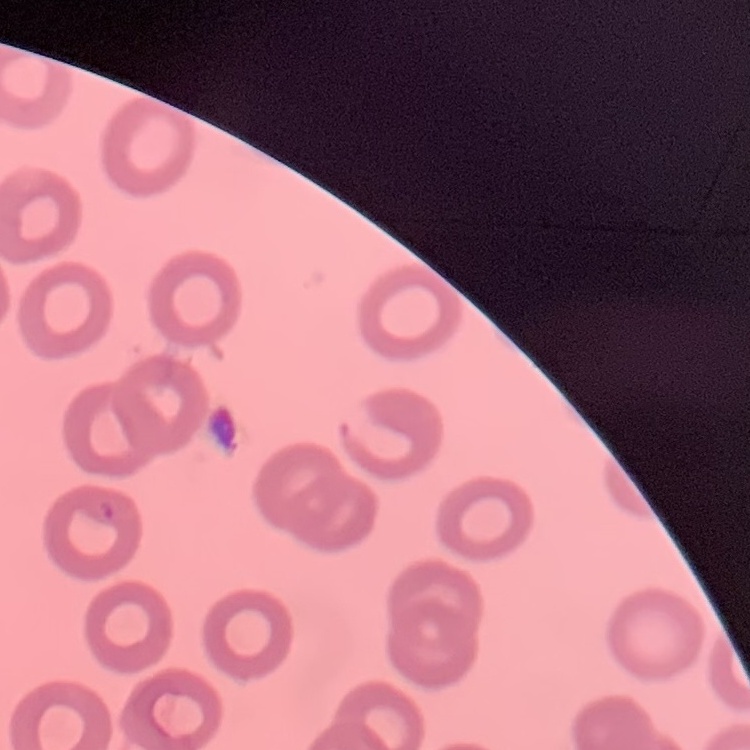

red blood cell morphology = no rouleaux formation
stain = Field's or Giemsa
image type = one tile cut from a larger photomicrograph
preparation = thin blood smear